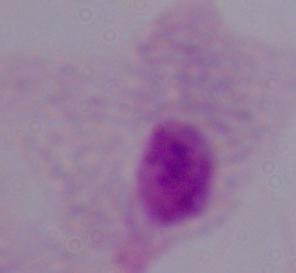
Summary:
  - Magnification: 1000x
  - Identification: trichomonad
  - Modality: micrograph